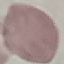 Result: negative for malaria parasites. Acquired by smartphone through the microscope eyepiece. Thin blood smear. Cell patch, automatically extracted from a larger field of view and resized to 64 × 64 pixels. Giemsa stain.